Comment on the morphology of the red blood cells.
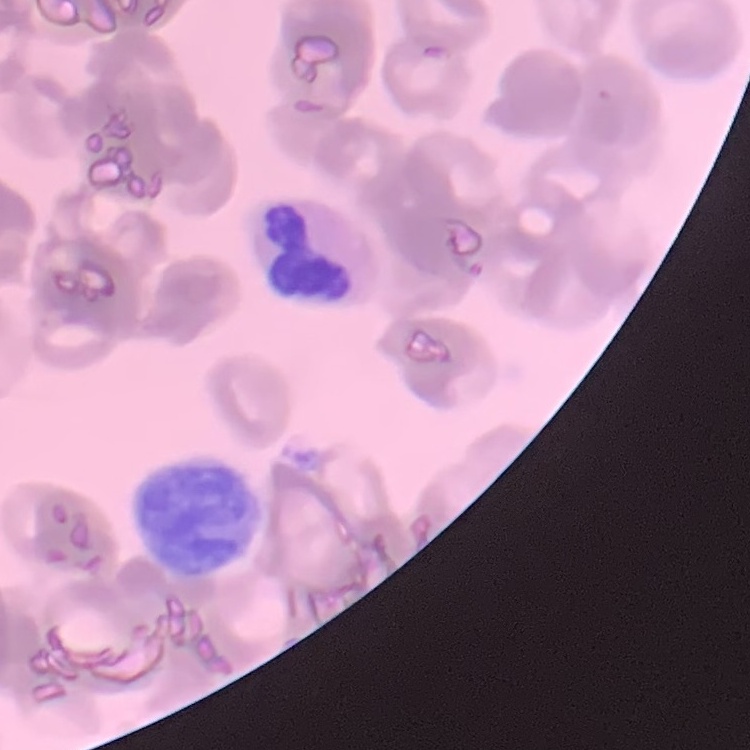
Rouleaux formation.

One tile cut from a larger photomicrograph. Thin peripheral smear. Field's or Giemsa stain.